Comment on the morphology of the red blood cells.
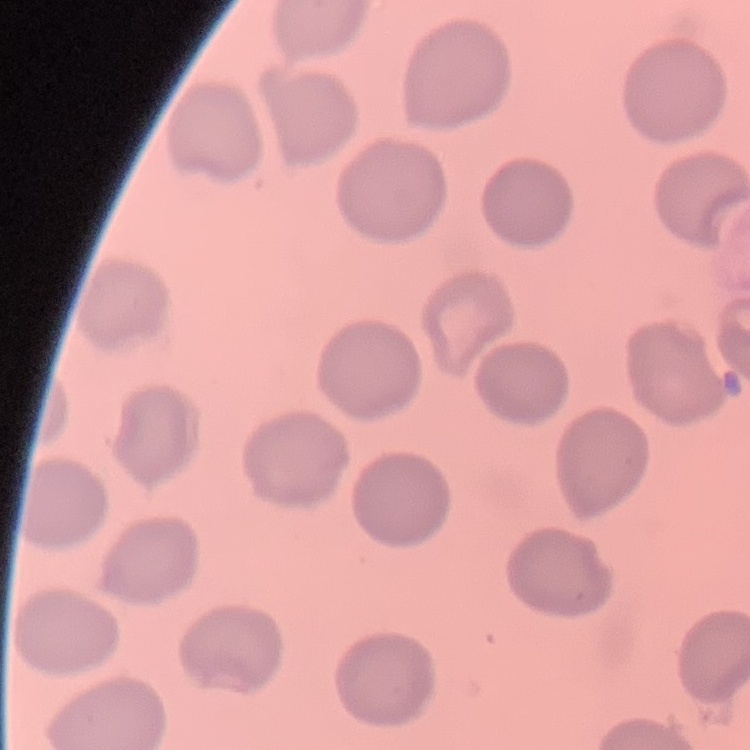

They show no rouleaux formation.

Summary:
  - Image type: one tile cut from a larger photomicrograph
  - Preparation: thin blood film
  - Stain: Field's or Giemsa